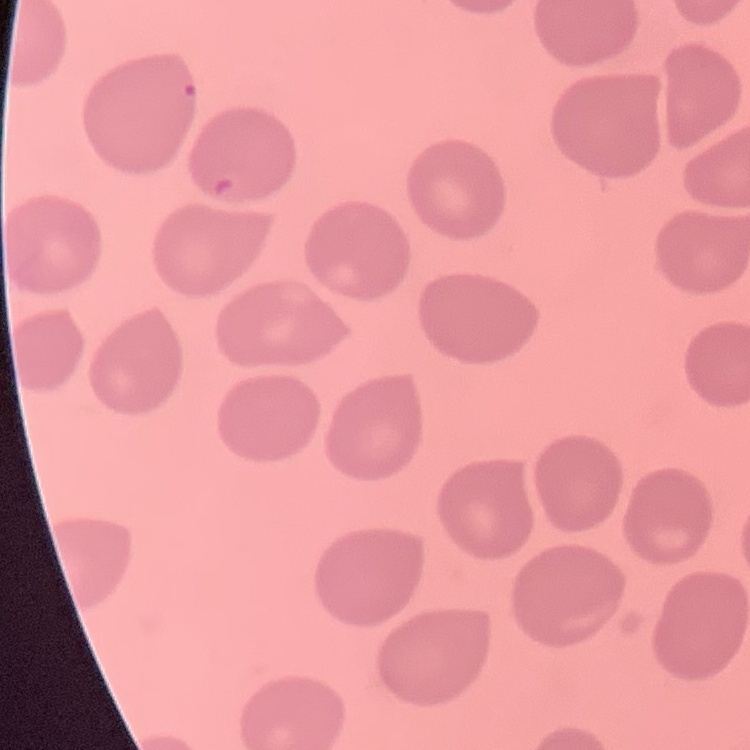
Summary:
  - Red blood cell morphology: no rouleaux formation
  - Stain: Field's or Giemsa
  - Image type: square crop of a larger photomicrograph
  - Preparation: thin blood film